Report the malaria status of this cell.
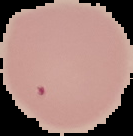

Uninfected.

image_type: segmented cell region with the area outside set to black
preparation: thin blood smear
image_size: 133×136 pixels